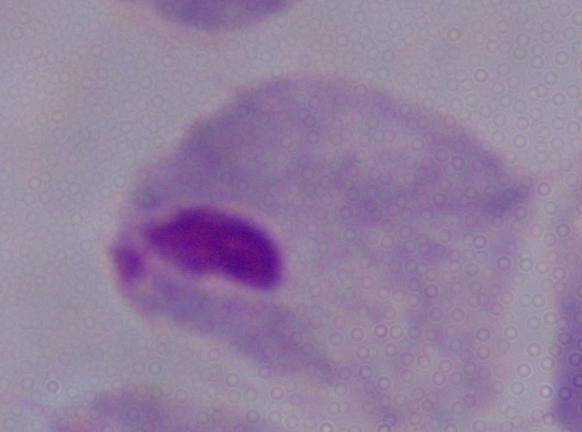 A trichomonad is shown. 1000x magnification. Micrograph.